Classify this cell by malaria status.
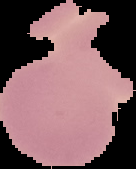
Uninfected.

Summary:
  - Preparation: thin blood film
  - Image type: segmented cell region with the area outside set to black
  - Image size: 136×169 pixels